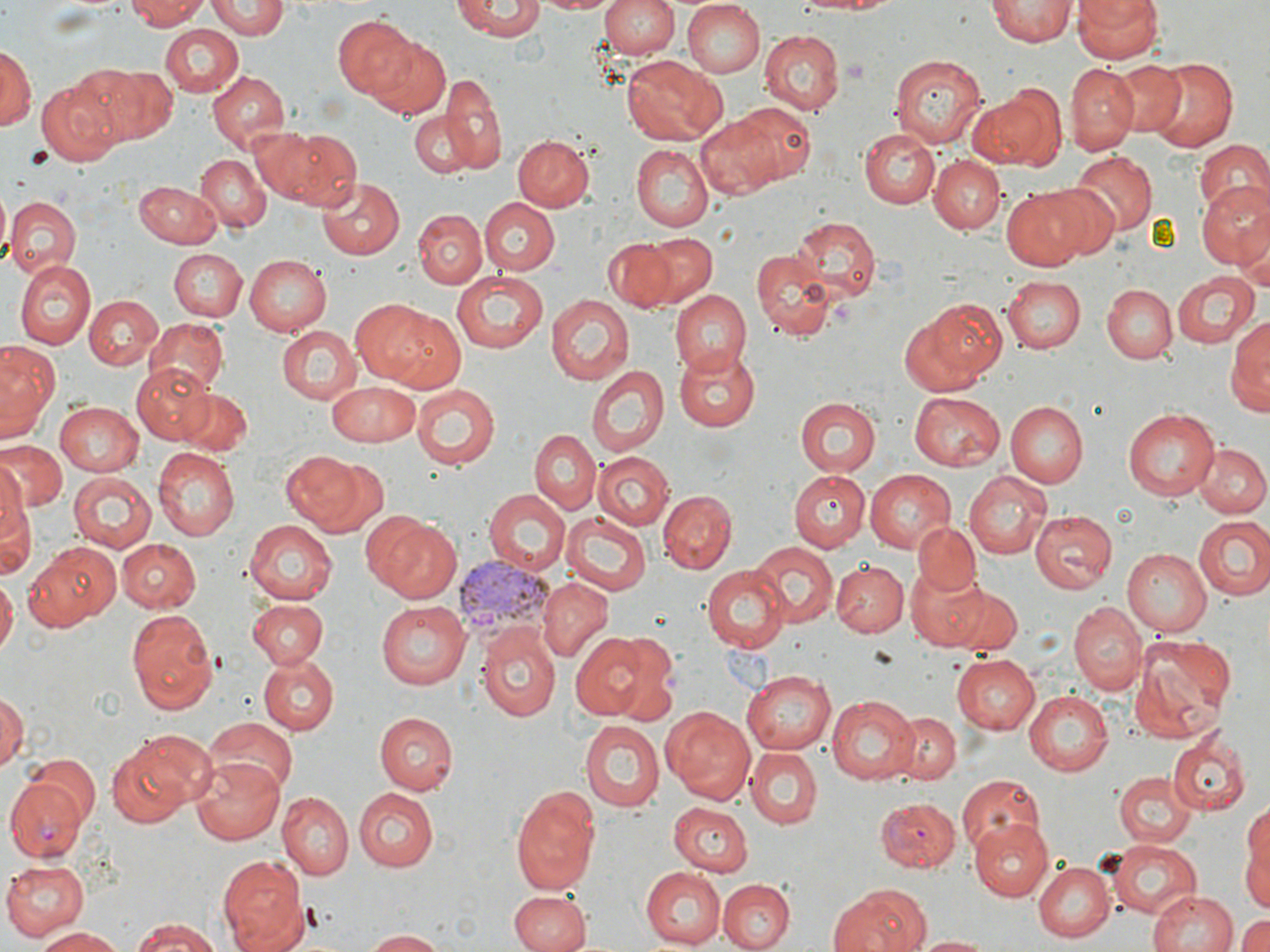

slide_level_diagnosis: Plasmodium vivax
modality: light microscopy
plasmodium_vivax_infected_red_blood_cell_locations: 'approximate bounding boxes as named x1/y1/x2/y2 corners in pixels: (x1=456, y1=556, x2=553, y2=639), (x1=6, y1=779, x2=88, y2=863), (x1=875, y1=798, x2=961, y2=869)'
preparation: thin blood smear
image_size: 1270×952 pixels
field_of_view: single
uninfected_red_blood_cell_locations: 'approximate bounding boxes as named x1/y1/x2/y2 corners in pixels: (x1=126, y1=0, x2=210, y2=28), (x1=206, y1=0, x2=287, y2=40), (x1=535, y1=0, x2=617, y2=15), (x1=601, y1=0, x2=680, y2=60), (x1=661, y1=0, x2=762, y2=144), (x1=793, y1=0, x2=904, y2=16), (x1=988, y1=0, x2=1076, y2=46), (x1=1073, y1=0, x2=1163, y2=64), (x1=453, y1=1, x2=544, y2=40), (x1=681, y1=1, x2=765, y2=78), (x1=332, y1=16, x2=420, y2=99), (x1=160, y1=25, x2=242, y2=98), (x1=758, y1=29, x2=844, y2=115), (x1=362, y1=34, x2=452, y2=120), (x1=0, y1=44, x2=35, y2=136), (x1=889, y1=52, x2=985, y2=148), (x1=622, y1=56, x2=723, y2=145), (x1=1143, y1=56, x2=1242, y2=154), (x1=1110, y1=60, x2=1186, y2=135), (x1=1065, y1=61, x2=1140, y2=151), (x1=91, y1=66, x2=175, y2=142), (x1=206, y1=70, x2=289, y2=154), (x1=438, y1=74, x2=505, y2=171), (x1=35, y1=80, x2=119, y2=165), (x1=969, y1=85, x2=1066, y2=171), (x1=725, y1=100, x2=817, y2=187), (x1=412, y1=114, x2=475, y2=178), (x1=693, y1=114, x2=782, y2=199), (x1=245, y1=126, x2=320, y2=201), (x1=858, y1=127, x2=939, y2=208), (x1=266, y1=128, x2=359, y2=209), (x1=513, y1=135, x2=595, y2=213), (x1=1195, y1=141, x2=1270, y2=223), (x1=631, y1=144, x2=714, y2=230), (x1=1067, y1=152, x2=1157, y2=237), (x1=195, y1=154, x2=270, y2=232), (x1=930, y1=157, x2=1004, y2=234), (x1=314, y1=175, x2=403, y2=261), (x1=135, y1=180, x2=223, y2=246), (x1=1197, y1=183, x2=1270, y2=272), (x1=1000, y1=185, x2=1093, y2=270), (x1=4, y1=195, x2=80, y2=277), (x1=478, y1=197, x2=559, y2=277), (x1=414, y1=209, x2=486, y2=289), (x1=791, y1=216, x2=878, y2=298), (x1=632, y1=230, x2=718, y2=308), (x1=604, y1=238, x2=674, y2=311), (x1=753, y1=247, x2=835, y2=340), (x1=168, y1=249, x2=247, y2=322), (x1=246, y1=253, x2=333, y2=336), (x1=13, y1=261, x2=95, y2=349), (x1=451, y1=271, x2=550, y2=354), (x1=1172, y1=271, x2=1258, y2=349), (x1=1000, y1=276, x2=1086, y2=355), (x1=1102, y1=283, x2=1177, y2=363), (x1=671, y1=289, x2=750, y2=375), (x1=84, y1=294, x2=161, y2=370), (x1=547, y1=294, x2=632, y2=385), (x1=354, y1=298, x2=450, y2=389), (x1=900, y1=301, x2=1004, y2=395), (x1=1230, y1=311, x2=1269, y2=413), (x1=143, y1=319, x2=227, y2=394), (x1=278, y1=325, x2=359, y2=404), (x1=0, y1=340, x2=58, y2=439), (x1=674, y1=344, x2=760, y2=432), (x1=132, y1=362, x2=213, y2=443), (x1=585, y1=363, x2=669, y2=459), (x1=328, y1=383, x2=422, y2=445), (x1=411, y1=384, x2=500, y2=470), (x1=174, y1=389, x2=254, y2=456), (x1=909, y1=391, x2=1004, y2=470), (x1=794, y1=398, x2=878, y2=477), (x1=1006, y1=400, x2=1088, y2=488), (x1=54, y1=402, x2=143, y2=474), (x1=1123, y1=407, x2=1221, y2=499), (x1=530, y1=429, x2=601, y2=514), (x1=0, y1=441, x2=66, y2=512), (x1=1194, y1=442, x2=1268, y2=518), (x1=283, y1=449, x2=380, y2=531), (x1=152, y1=450, x2=239, y2=540), (x1=595, y1=452, x2=672, y2=530), (x1=0, y1=460, x2=28, y2=537), (x1=865, y1=470, x2=956, y2=552), (x1=963, y1=470, x2=1051, y2=561), (x1=790, y1=471, x2=870, y2=550), (x1=67, y1=473, x2=154, y2=555), (x1=484, y1=489, x2=570, y2=576), (x1=658, y1=490, x2=736, y2=573), (x1=0, y1=491, x2=36, y2=581), (x1=357, y1=509, x2=432, y2=592), (x1=1028, y1=510, x2=1115, y2=594), (x1=563, y1=513, x2=653, y2=594), (x1=1194, y1=514, x2=1270, y2=599), (x1=375, y1=519, x2=463, y2=604), (x1=245, y1=522, x2=337, y2=603), (x1=912, y1=522, x2=981, y2=596), (x1=118, y1=538, x2=201, y2=611), (x1=749, y1=540, x2=836, y2=627), (x1=20, y1=541, x2=120, y2=632), (x1=1121, y1=549, x2=1211, y2=635), (x1=831, y1=559, x2=905, y2=637), (x1=903, y1=564, x2=989, y2=649), (x1=702, y1=565, x2=790, y2=653), (x1=0, y1=576, x2=17, y2=653), (x1=537, y1=577, x2=612, y2=660), (x1=944, y1=584, x2=1023, y2=655), (x1=246, y1=598, x2=329, y2=668), (x1=375, y1=601, x2=469, y2=688), (x1=1069, y1=601, x2=1146, y2=695), (x1=128, y1=607, x2=216, y2=714), (x1=476, y1=623, x2=560, y2=721), (x1=567, y1=633, x2=655, y2=720), (x1=1130, y1=638, x2=1233, y2=742), (x1=609, y1=645, x2=678, y2=727), (x1=949, y1=653, x2=1039, y2=734), (x1=259, y1=654, x2=338, y2=735), (x1=740, y1=669, x2=835, y2=754), (x1=0, y1=690, x2=25, y2=773), (x1=1024, y1=690, x2=1113, y2=774), (x1=826, y1=694, x2=918, y2=784), (x1=663, y1=705, x2=756, y2=805), (x1=365, y1=710, x2=452, y2=867), (x1=891, y1=712, x2=961, y2=785), (x1=375, y1=713, x2=456, y2=793), (x1=204, y1=718, x2=296, y2=800), (x1=581, y1=720, x2=664, y2=811), (x1=1167, y1=733, x2=1249, y2=814), (x1=107, y1=734, x2=204, y2=827), (x1=744, y1=747, x2=823, y2=829), (x1=26, y1=754, x2=102, y2=830), (x1=192, y1=754, x2=289, y2=844), (x1=1114, y1=772, x2=1195, y2=848), (x1=956, y1=775, x2=1046, y2=854), (x1=510, y1=784, x2=600, y2=894), (x1=354, y1=787, x2=437, y2=872), (x1=278, y1=792, x2=351, y2=879), (x1=667, y1=801, x2=752, y2=877), (x1=1244, y1=802, x2=1269, y2=901), (x1=966, y1=819, x2=1053, y2=901), (x1=1107, y1=839, x2=1203, y2=918), (x1=216, y1=852, x2=307, y2=952), (x1=0, y1=858, x2=88, y2=940), (x1=1033, y1=861, x2=1113, y2=942), (x1=643, y1=867, x2=726, y2=949), (x1=717, y1=877, x2=792, y2=952), (x1=830, y1=883, x2=931, y2=952), (x1=1147, y1=889, x2=1238, y2=952), (x1=509, y1=892, x2=588, y2=952), (x1=1235, y1=912, x2=1270, y2=952), (x1=126, y1=918, x2=224, y2=951), (x1=36, y1=927, x2=127, y2=951), (x1=364, y1=930, x2=450, y2=951), (x1=911, y1=935, x2=995, y2=951)'
stain: May-Grünwald-Giemsa
magnification: 1000x